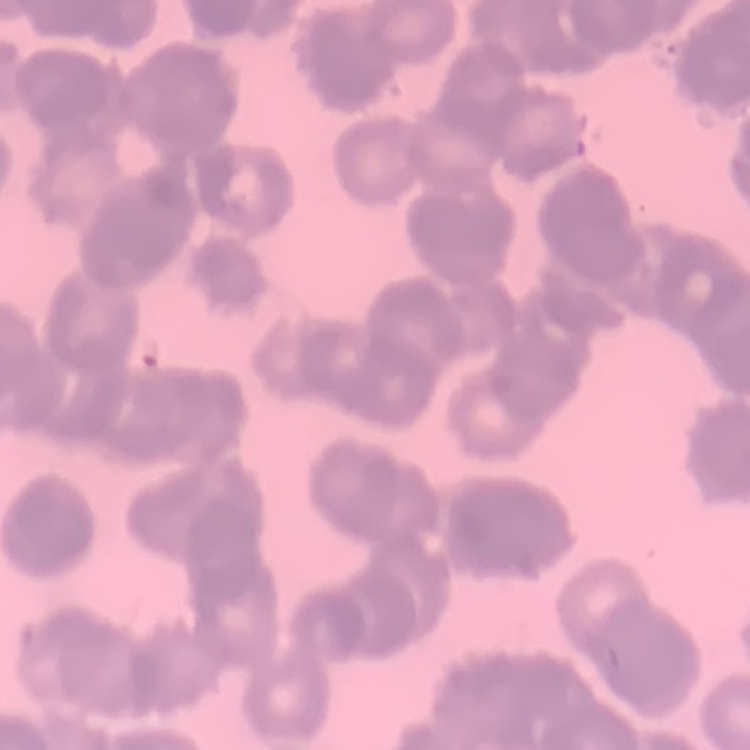
red blood cell morphology = rouleaux formation
preparation = thin peripheral smear
stain = Field's or Giemsa
image type = square crop of a larger photomicrograph